Describe the morphology of the red blood cells.
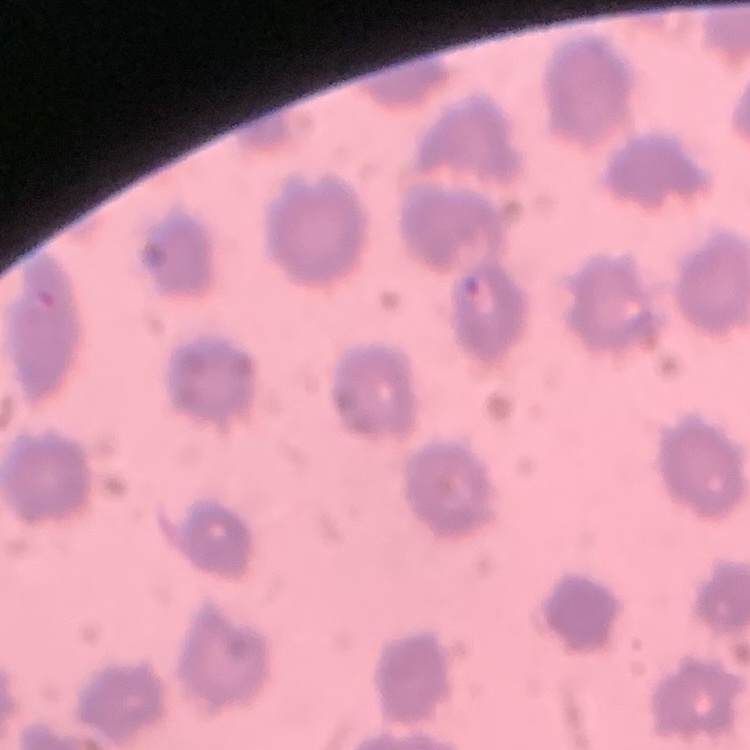

They show no rouleaux formation.

{
  "image_type": "one tile cut from a larger photomicrograph",
  "preparation": "thin blood smear",
  "stain": "Field's or Giemsa"
}